Assess for malaria.
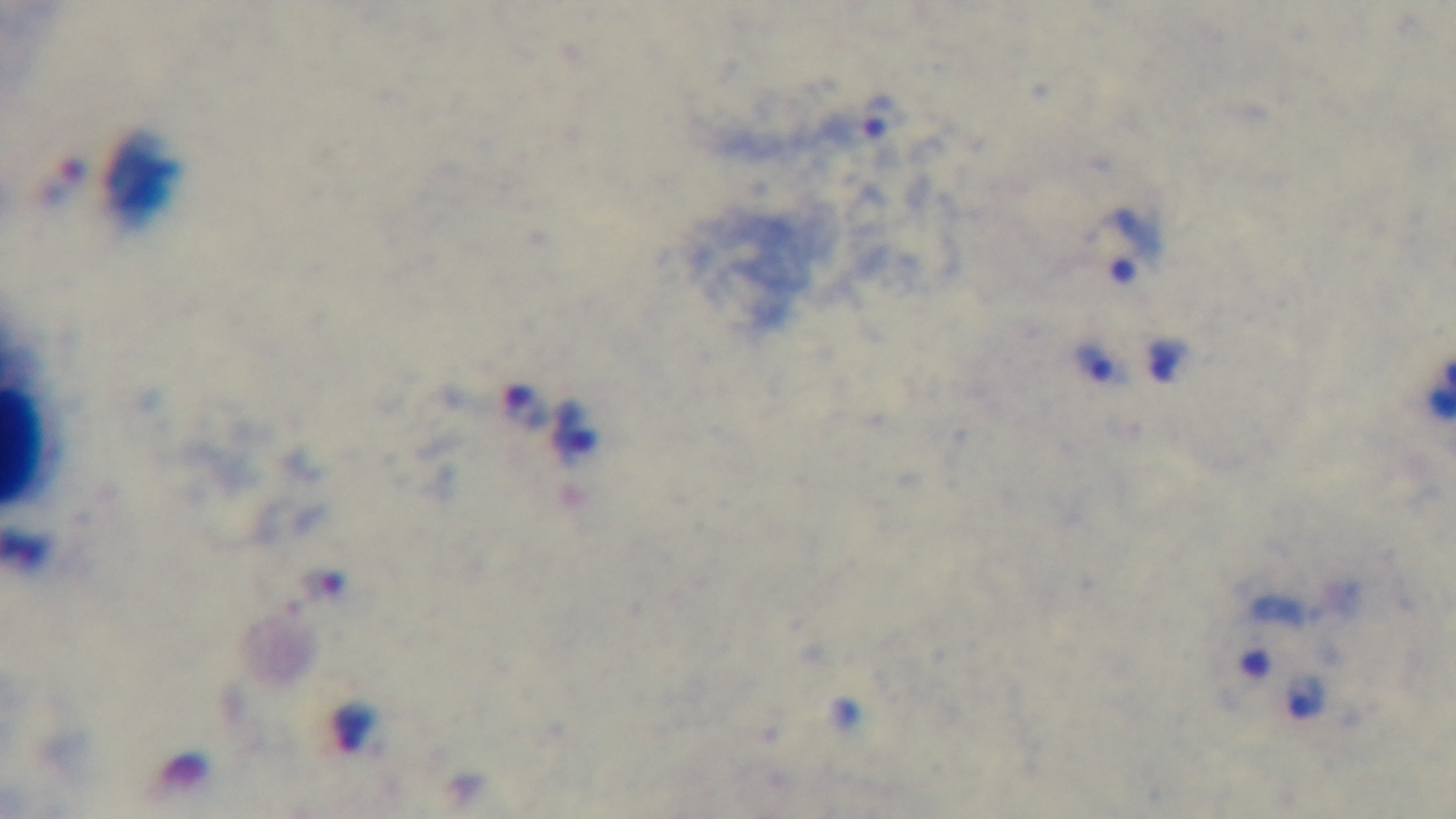
Infected.

Summary:
  - Capture: mounted 4K digital camera
  - Preparation: thick blood film
  - Stain: Giemsa
  - Modality: light microscopy
  - Objective: 100x oil immersion
  - Field of view: one from the slide